State which parasite is depicted.
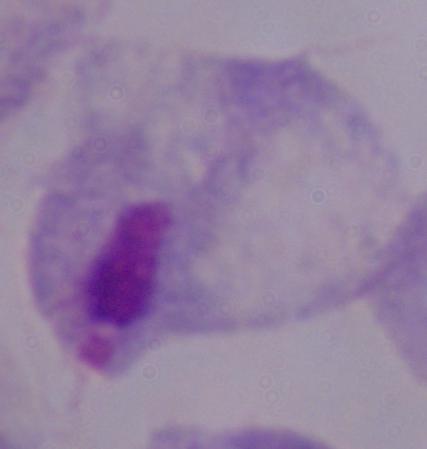
A trichomonad.

Summary:
  - Modality: photomicrograph
  - Magnification: 1000x